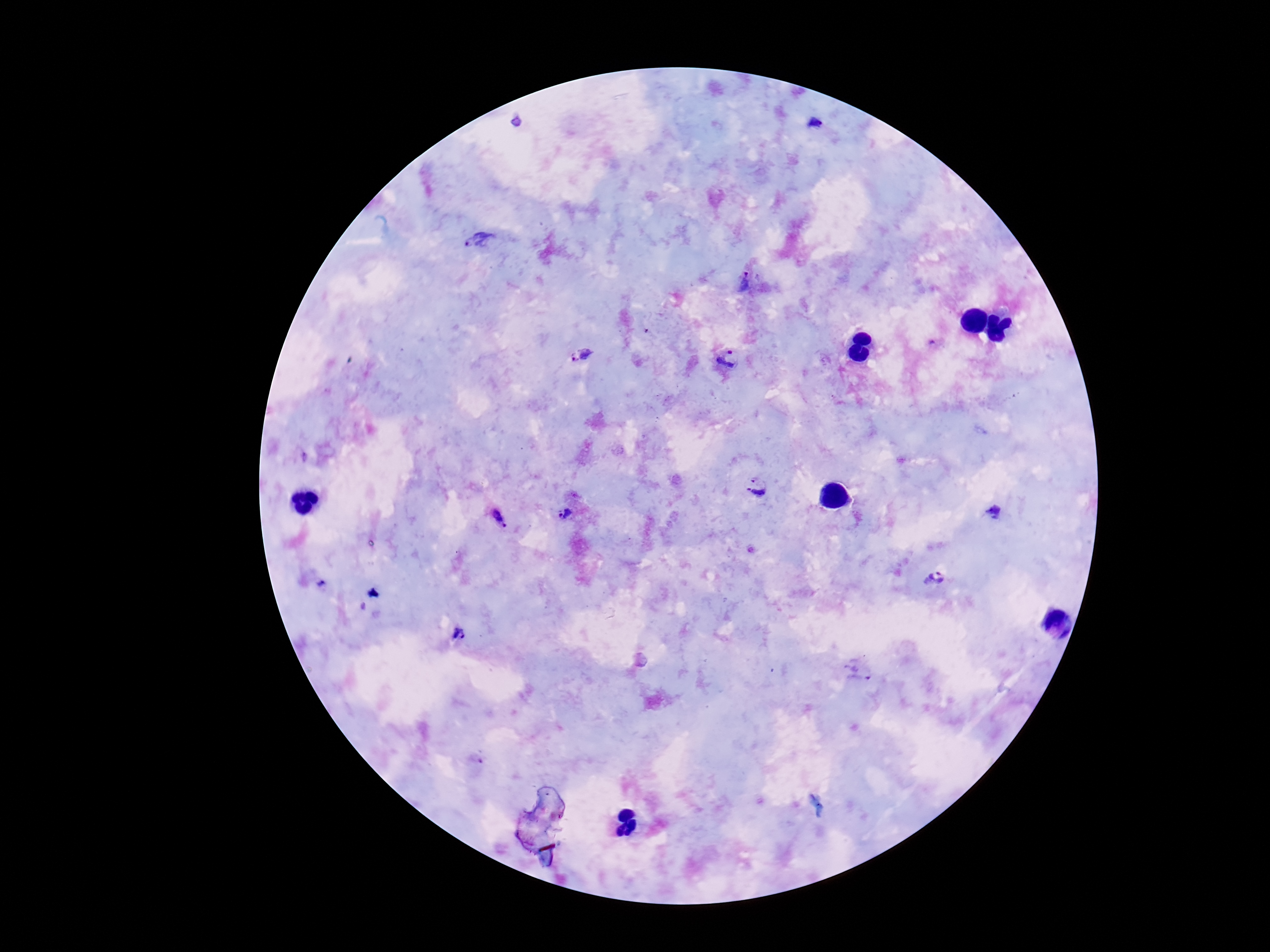
preparation = thick blood smear
capture = smartphone camera through the microscope eyepiece
Plasmodium parasite locations = approximate object centers, in pixels from the top-left corner: (x=814, y=123), (x=481, y=240), (x=745, y=285), (x=579, y=356), (x=730, y=358), (x=757, y=484), (x=564, y=514), (x=499, y=518), (x=934, y=577), (x=458, y=633), (x=860, y=670)
stain = Giemsa
field of view = one from this slide
patient malaria status = infected
image size = 1270×952 pixels
magnification = 100x